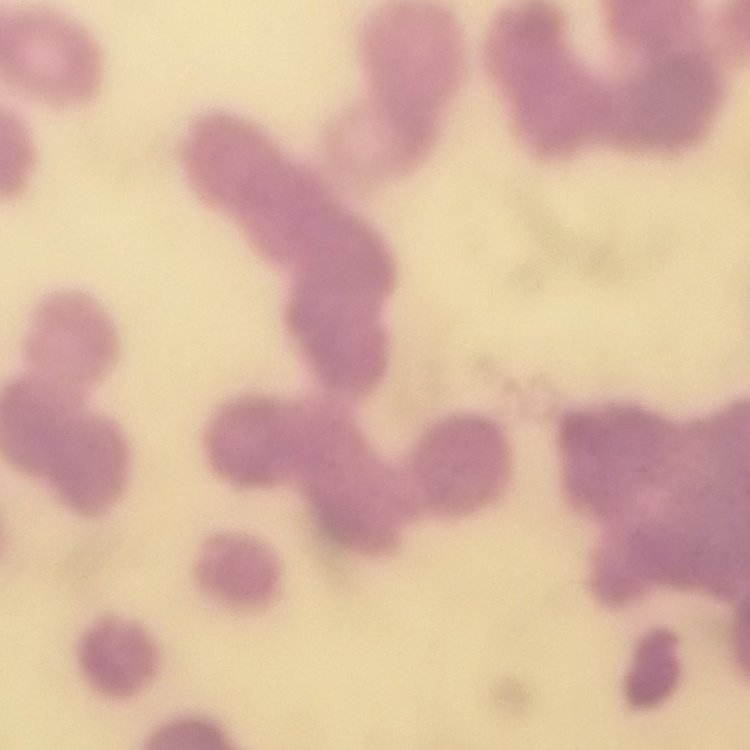

The erythrocytes exhibit rouleaux formation. Field's or Giemsa stain. One tile cut from a larger photomicrograph. Thin blood film.